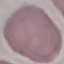

Result: no malaria parasites seen. Thin blood smear. Acquired by smartphone through the microscope eyepiece. Giemsa-stained preparation. Automatically extracted cell patch, resized to 64 × 64 pixels.